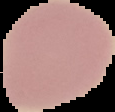

From a thin blood smear. Malaria status: uninfected. The area outside the segmented cell region is set to black. Image is 115×112 pixels.